State which parasite is depicted.
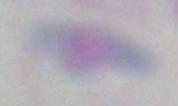
This is Toxoplasma gondii.

{
  "modality": "micrograph",
  "magnification": "1000x"
}